Report the malaria status of this cell.
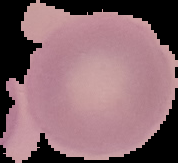
It is uninfected.

Image is 178×163 pixels. From a thin blood smear. The area outside the segmented cell region is set to black.